Name the blood parasite species.
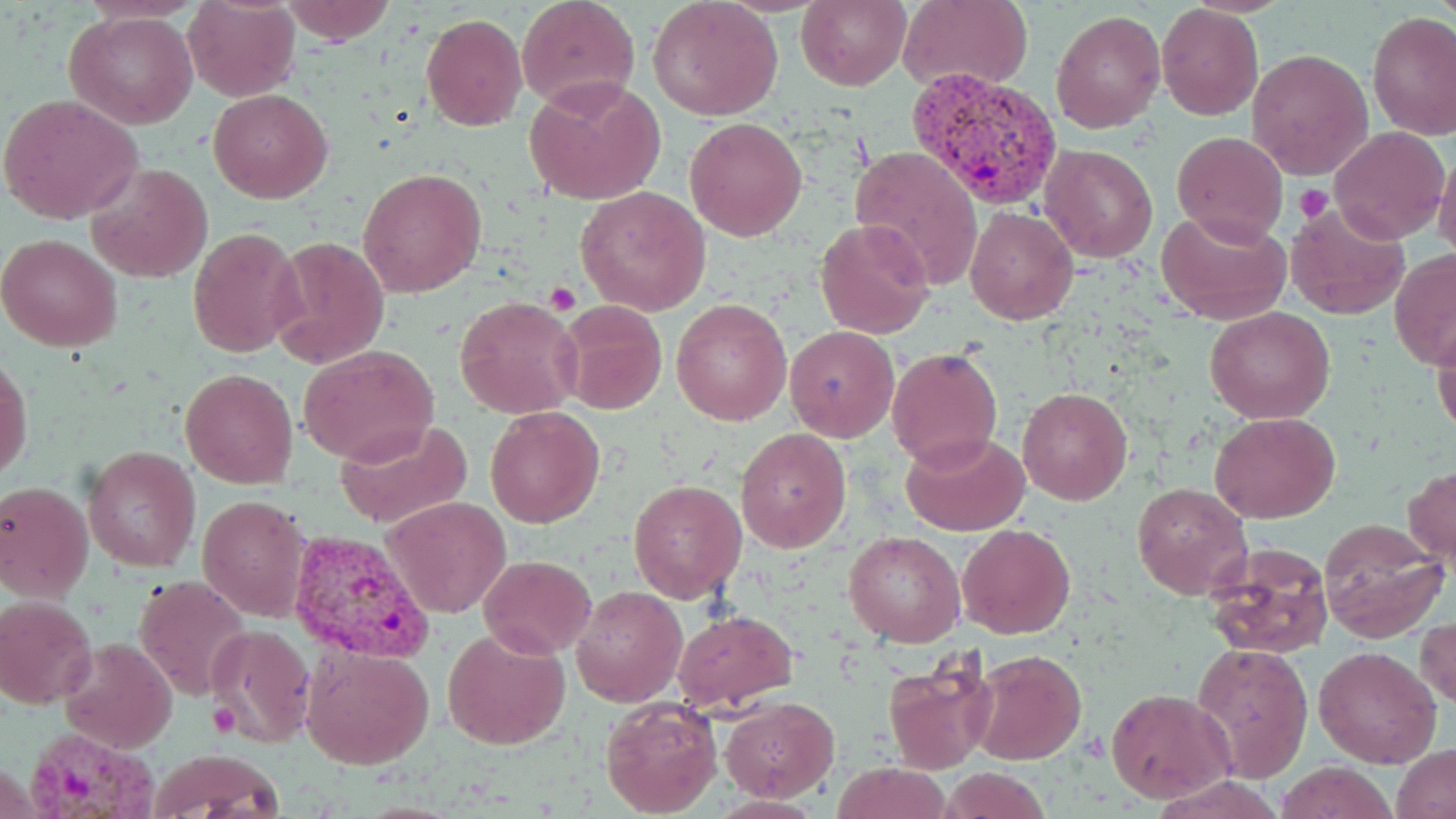

Plasmodium vivax.

Approximate bounding boxes as (x1,y1)-(x2,y2) corner pairs in pixels. Plasmodium vivax-infected red blood cell locations: (912,65)-(1065,211), (286,528)-(435,664), (21,725)-(169,817). Uninfected red blood cell locations: (182,0)-(300,101), (278,0)-(398,45), (516,0)-(639,112), (647,0)-(783,121), (796,0)-(911,90), (898,0)-(1032,91), (1156,4)-(1263,119), (1049,9)-(1166,134), (66,10)-(198,128), (1367,11)-(1456,140), (420,13)-(528,132), (1247,49)-(1373,180), (524,76)-(665,205), (209,89)-(332,203), (1,94)-(145,226), (685,117)-(809,240), (1331,126)-(1449,243), (1172,131)-(1288,245), (1041,144)-(1158,264), (850,145)-(984,291), (1432,146)-(1456,261), (86,161)-(213,284), (358,167)-(487,297), (575,186)-(711,315), (1285,203)-(1410,319), (965,206)-(1078,324), (1156,210)-(1291,324), (815,218)-(935,338), (188,225)-(303,357), (0,233)-(123,352), (270,237)-(389,368), (1390,250)-(1456,369), (454,295)-(582,419), (671,296)-(792,426), (558,301)-(666,415), (1204,306)-(1334,423), (1432,316)-(1456,440), (784,326)-(899,442), (299,344)-(439,465), (887,347)-(1003,468), (1,354)-(33,485), (180,368)-(298,489), (1017,387)-(1132,504), (485,406)-(605,528), (1212,411)-(1339,524), (333,419)-(475,531), (736,428)-(849,551), (900,429)-(1028,535), (82,445)-(200,571), (1405,465)-(1455,567), (0,479)-(94,602), (628,480)-(747,601), (1132,482)-(1254,600), (199,495)-(308,619), (385,497)-(510,619), (1316,517)-(1449,641), (958,522)-(1075,639), (843,530)-(965,646), (1203,541)-(1335,659), (479,554)-(594,657), (134,576)-(251,701), (570,585)-(687,705), (0,595)-(99,707), (672,608)-(799,712), (1416,617)-(1455,709), (207,624)-(316,746), (442,627)-(570,750), (59,639)-(178,753), (1191,639)-(1313,784), (1312,644)-(1443,769), (303,645)-(434,769), (971,650)-(1087,766), (880,653)-(999,775), (1107,687)-(1236,803), (598,695)-(723,818), (720,696)-(838,802), (1393,743)-(1456,819), (149,750)-(285,818), (1274,760)-(1400,819), (832,763)-(951,819), (942,766)-(1051,819), (709,796)-(826,818). Platelet locations: (1296,186)-(1333,223), (543,282)-(579,314). 1000x magnification. One field of a larger specimen. Light microscopy. Image is 1456×819 pixels. Thin blood smear. May-Grünwald-Giemsa-stained preparation.